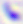

Summary:
  - Modality: photomicrograph
  - Identification: Toxoplasma gondii
  - Magnification: 400x